Name the blood parasite species.
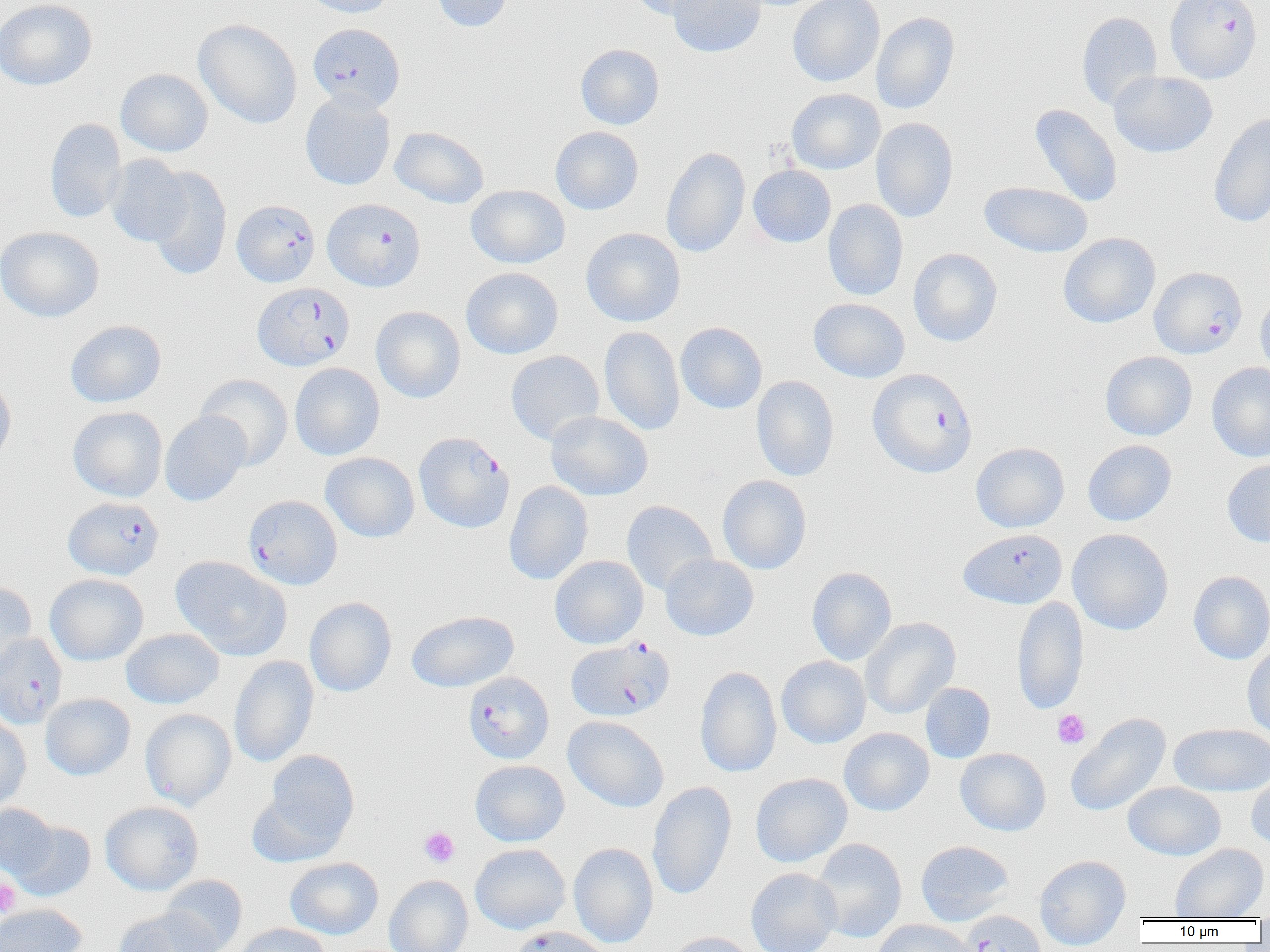
Plasmodium falciparum.

uninfected red blood cell locations (subset) = approximate bounding boxes as [x1, y1, x2, y2] in pixels: [0, 0, 97, 91], [301, 0, 396, 19], [429, 0, 513, 32], [626, 0, 720, 20], [668, 0, 766, 58], [788, 0, 885, 87], [1076, 11, 1162, 110], [871, 12, 959, 114], [194, 18, 302, 129], [576, 43, 664, 130], [115, 69, 213, 156], [1107, 71, 1217, 158], [786, 88, 885, 174], [300, 92, 396, 191], [1029, 104, 1123, 207], [1208, 113, 1270, 228], [870, 117, 958, 222], [44, 118, 127, 223], [550, 126, 644, 215], [390, 127, 489, 208], [661, 147, 750, 258], [104, 155, 193, 247], [144, 165, 233, 281], [748, 165, 836, 248], [979, 181, 1093, 258], [466, 185, 570, 269], [823, 199, 908, 300], [0, 225, 104, 322], [581, 227, 685, 327], [1057, 233, 1160, 328], [908, 248, 1002, 346], [461, 267, 563, 359], [1255, 292, 1270, 381], [808, 298, 910, 383], [370, 306, 466, 402], [65, 320, 166, 408], [675, 322, 767, 413], [599, 326, 685, 435], [506, 350, 604, 445], [1100, 351, 1197, 441], [1206, 362, 1270, 462], [289, 363, 384, 460], [0, 374, 17, 468], [195, 374, 293, 470], [751, 376, 840, 481], [68, 406, 167, 502], [545, 411, 653, 501], [159, 412, 250, 506], [1083, 440, 1176, 526], [970, 442, 1070, 532], [320, 452, 420, 542], [1221, 458, 1270, 547], [717, 475, 812, 574], [504, 481, 594, 585], [621, 501, 718, 595], [1067, 528, 1173, 635], [660, 553, 758, 641], [549, 555, 649, 648], [171, 556, 291, 660], [806, 566, 897, 666], [1188, 571, 1270, 664], [44, 573, 148, 666], [0, 582, 37, 678], [1012, 595, 1089, 715], [304, 597, 397, 697], [406, 610, 519, 693], [861, 617, 961, 719], [121, 628, 223, 709], [1242, 643, 1270, 739], [229, 655, 319, 767], [776, 656, 870, 748], [695, 666, 782, 777], [921, 683, 995, 763], [40, 693, 136, 780], [139, 709, 236, 810], [1065, 713, 1171, 817], [0, 714, 31, 810], [563, 716, 669, 812], [1169, 723, 1270, 796], [839, 727, 934, 816], [955, 748, 1051, 836], [259, 749, 360, 855], [470, 759, 569, 847], [1246, 768, 1270, 849], [750, 773, 853, 868], [647, 781, 737, 900], [1123, 782, 1226, 860], [100, 801, 204, 895], [0, 803, 60, 881], [10, 819, 96, 901], [811, 838, 907, 942], [915, 840, 1014, 926], [470, 843, 570, 934], [569, 843, 658, 947], [1170, 843, 1268, 920], [1034, 854, 1131, 950], [285, 857, 384, 939], [746, 867, 841, 952], [160, 874, 247, 952], [384, 875, 473, 952], [0, 904, 87, 952], [113, 909, 220, 952], [870, 920, 977, 952], [232, 923, 330, 952], [664, 931, 760, 952]
image size = 1270×952 pixels
modality = optical microscopy
Plasmodium falciparum-infected red blood cell locations (subset) = approximate bounding boxes as [x1, y1, x2, y2] in pixels: [307, 23, 405, 112], [322, 198, 426, 291], [231, 200, 320, 288], [1154, 271, 1252, 363], [253, 282, 355, 371], [867, 368, 978, 478], [414, 431, 514, 533], [243, 495, 342, 590], [63, 496, 164, 580], [958, 528, 1067, 609], [0, 631, 66, 727], [566, 637, 675, 723], [463, 671, 554, 764], [957, 910, 1046, 952]
preparation = thin blood film
magnification = 1000x
field of view = single
platelet locations = approximate bounding boxes as [x1, y1, x2, y2] in pixels: [1052, 709, 1091, 749], [419, 827, 460, 867], [0, 878, 21, 918]